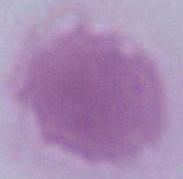

magnification = 1000x
modality = photomicrograph
identification = erythrocyte